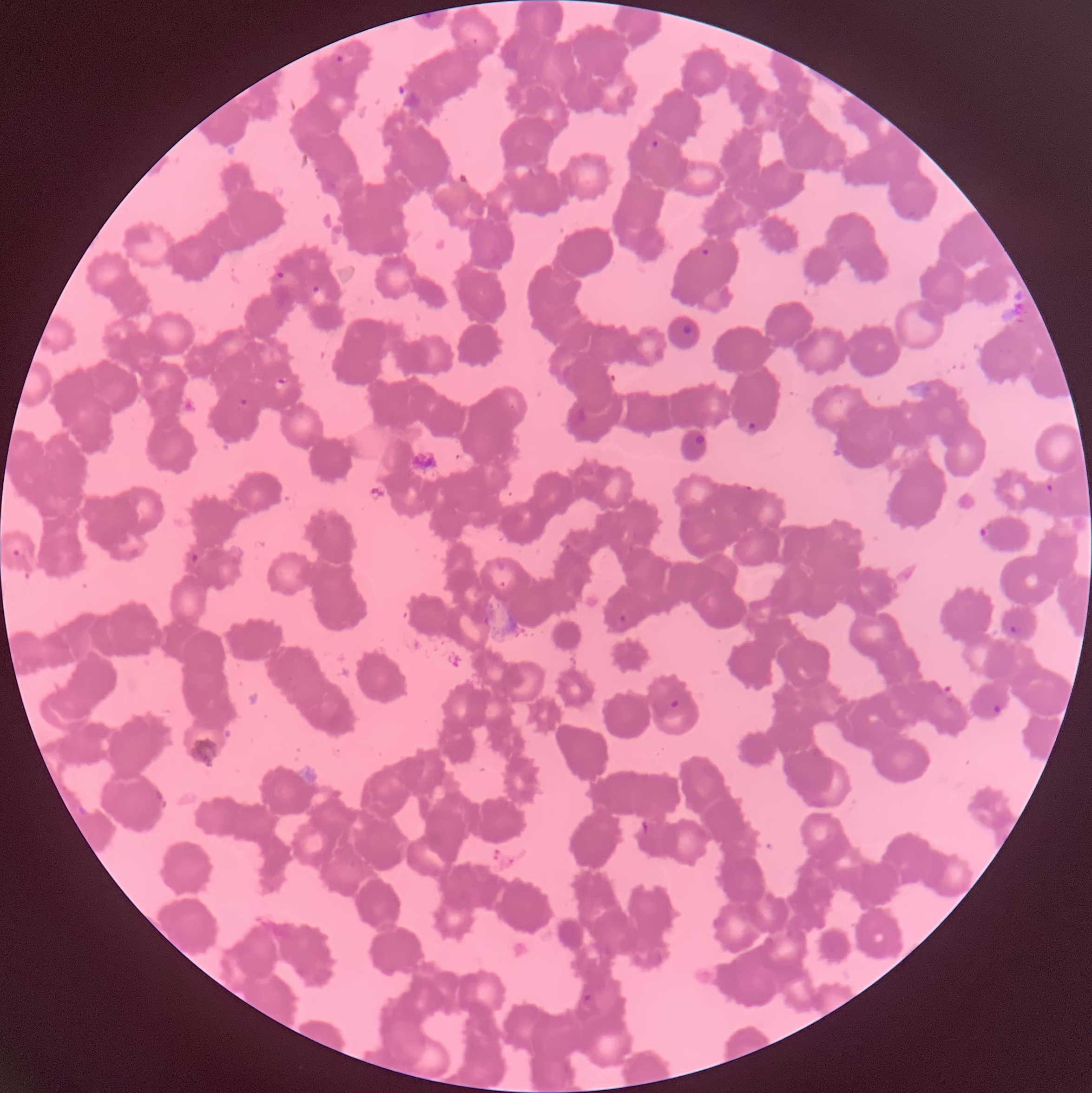
Approximate bounding boxes as [x1, y1, x2, y2] in pixels. Plasmodium parasite locations: [423, 11, 435, 20], [333, 52, 347, 67], [645, 138, 661, 153], [700, 247, 710, 257], [269, 266, 288, 281], [307, 282, 328, 304], [272, 377, 289, 391], [237, 397, 251, 409], [743, 418, 760, 435], [1044, 482, 1056, 493], [980, 527, 989, 538], [10, 548, 22, 559], [190, 553, 201, 565], [616, 613, 631, 625], [1010, 624, 1023, 635], [668, 698, 682, 710], [991, 703, 1004, 718], [579, 991, 595, 1006]. The red blood cells show rouleaux formation. Thin blood film. Image is 1092×1093 pixels. Optical microscopy.